Comment on the morphology of the red blood cells.
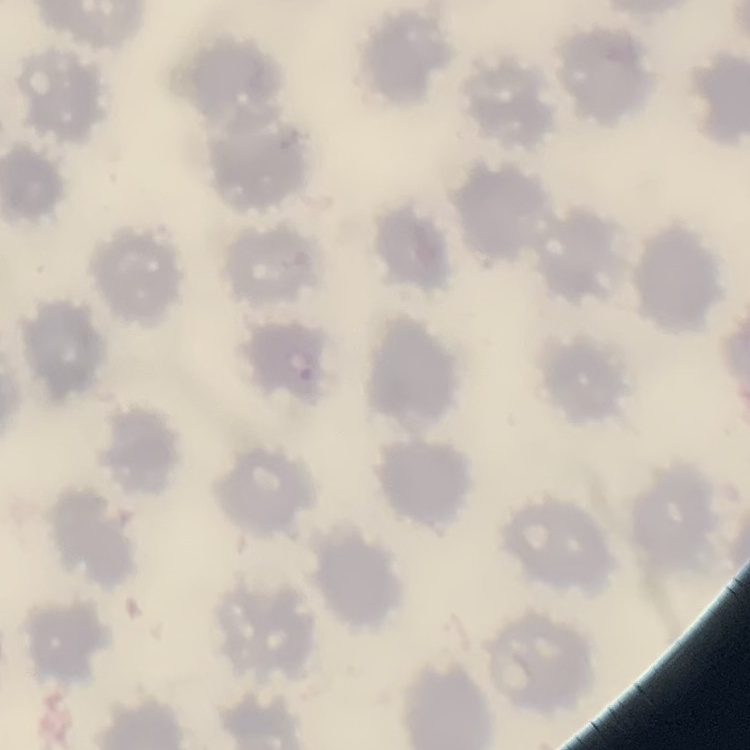
No rouleaux formation.

Stained with either Field's or Giemsa. Thin blood smear. Square crop of a larger photomicrograph.